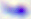
magnification = 400x
identification = Toxoplasma gondii
modality = photomicrograph